Describe the morphology of the red blood cells.
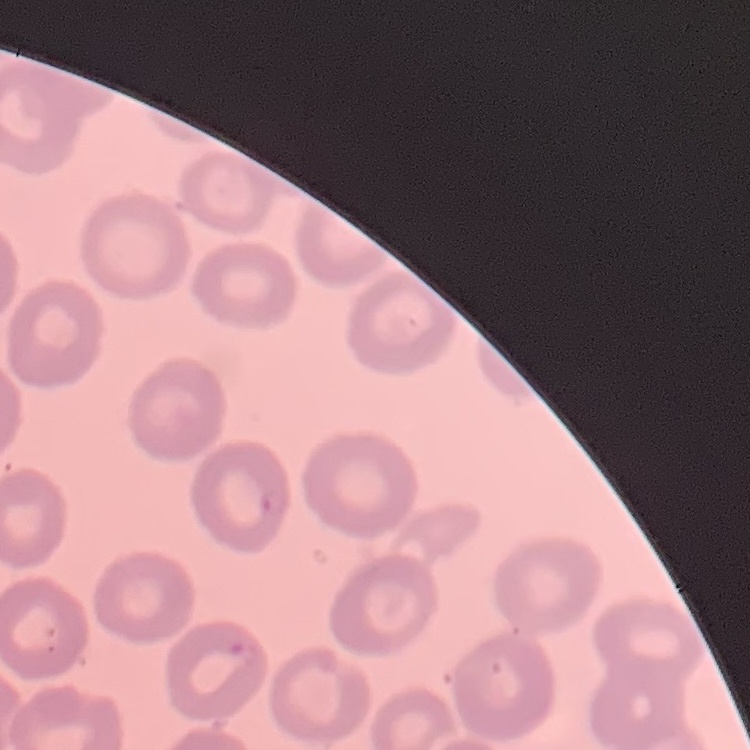

No rouleaux formation.

Summary:
  - Preparation: thin blood film
  - Stain: Field's or Giemsa
  - Image type: one tile cut from a larger photomicrograph